Give the preparation type.
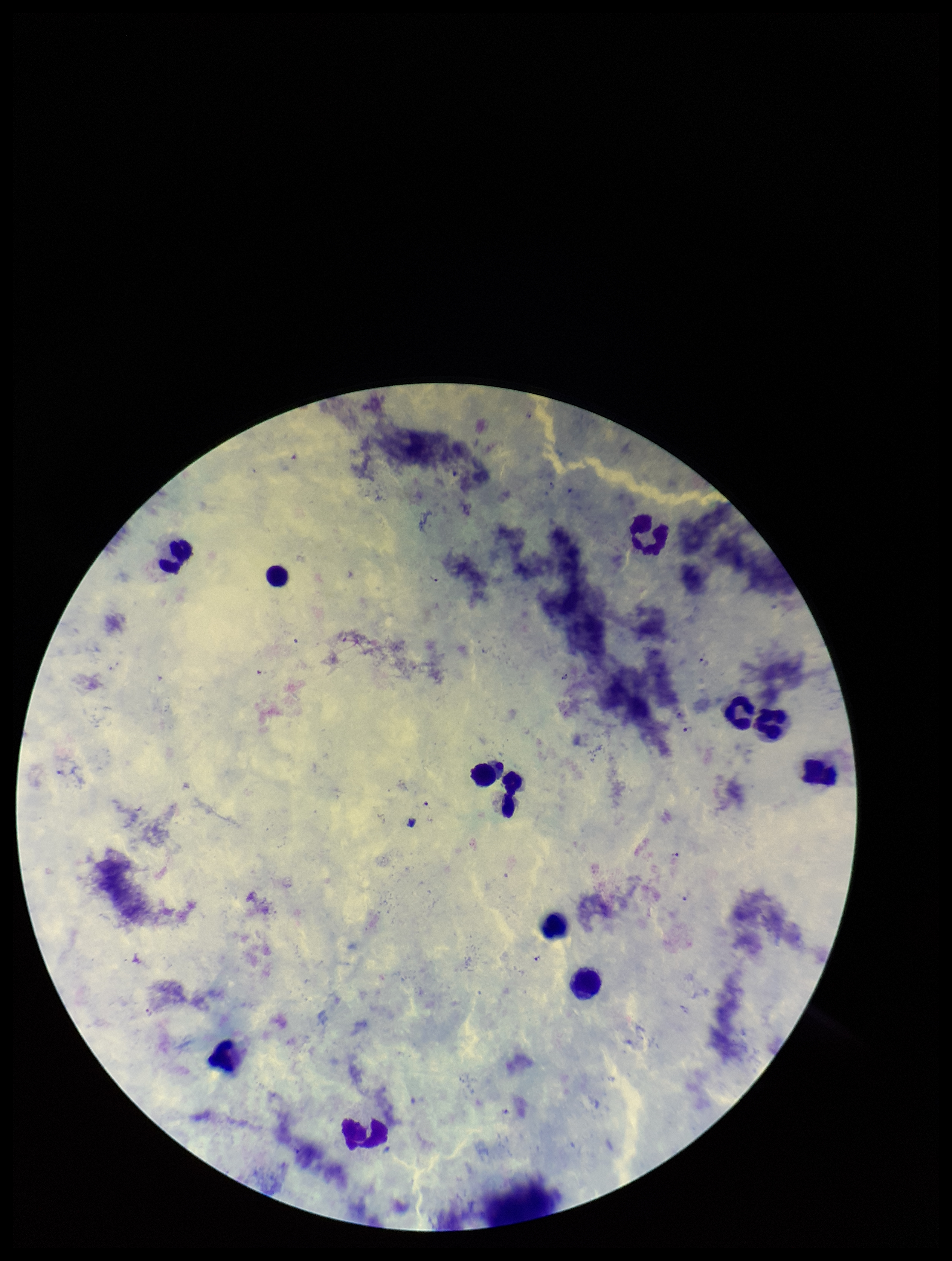
A thick smear.

Summary:
  - Species reported for this patient: Plasmodium falciparum
  - Patient malaria status: positive
  - Plasmodium parasites: seen
  - Stain: Giemsa
  - Image size: 952×1261 pixels
  - Field of view: single
  - Leukocyte count: 12
  - Parasite count: 6
  - Capture: smartphone photograph through the microscope eyepiece